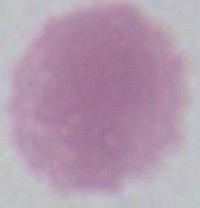
Summary:
  - Identification: red blood cell
  - Modality: photomicrograph
  - Magnification: 1000x